Comment on the morphology of the red blood cells.
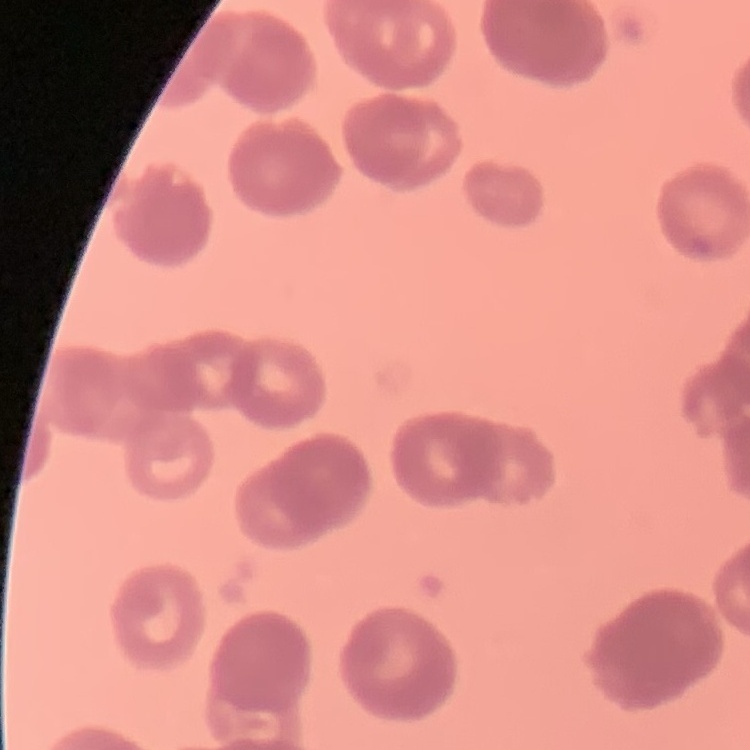
Rouleaux formation.

stain = Field's or Giemsa
image type = one tile cut from a larger photomicrograph
preparation = thin blood film